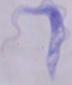
{
  "identification": "trypanosome",
  "magnification": "1000x",
  "modality": "micrograph"
}